Report the malaria status of this cell.
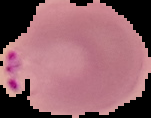

It is parasitized.

Summary:
  - Image type: segmented cell region on a black background
  - Image size: 151×118 pixels
  - Preparation: thin blood smear